Assess the morphology of the red blood cells.
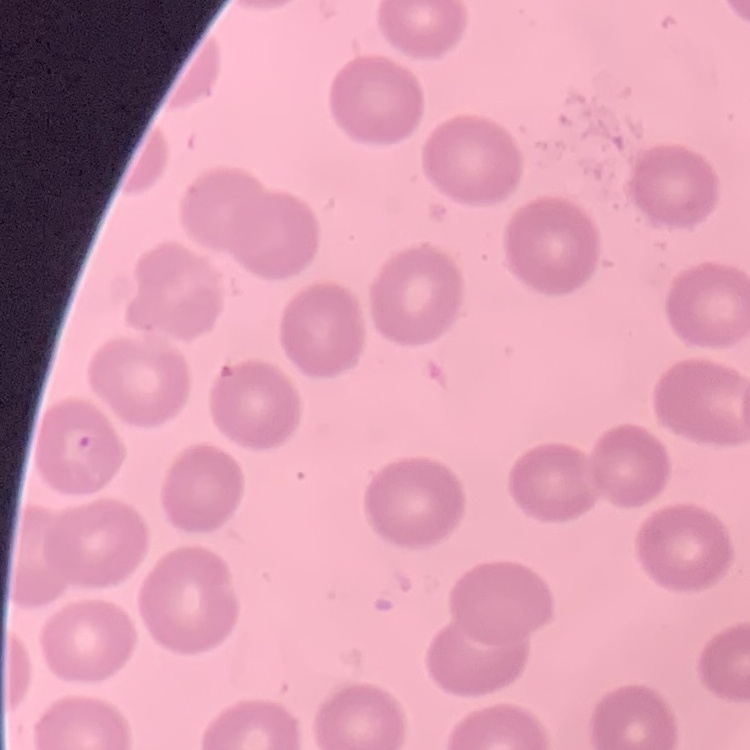
No rouleaux formation.

Summary:
  - Preparation: thin peripheral smear
  - Image type: square crop of a larger photomicrograph
  - Stain: Field's or Giemsa